Give the extent of all uninfected red blood cells.
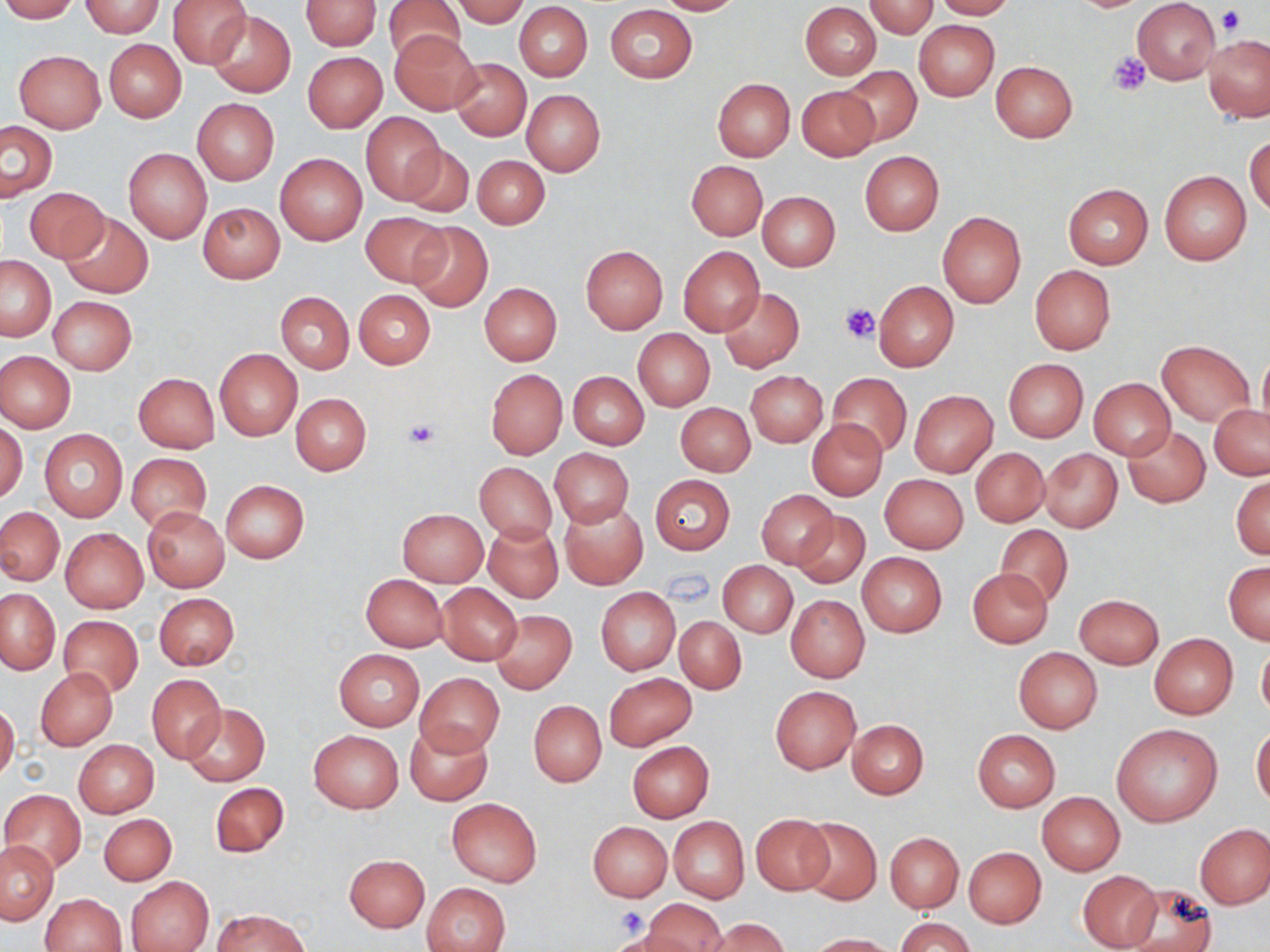
Approximate bounding boxes as [x1, y1, x2, y2] in pixels.
Uninfected red blood cells: [0, 0, 79, 22], [168, 0, 253, 69], [385, 0, 465, 66], [453, 0, 529, 26], [654, 0, 742, 15], [932, 0, 1016, 19], [1133, 0, 1221, 85], [82, 1, 164, 37], [300, 1, 381, 50], [864, 1, 936, 38], [514, 3, 592, 81], [800, 3, 882, 80], [605, 4, 698, 83], [206, 9, 296, 99], [914, 19, 999, 101], [390, 32, 481, 114], [1203, 34, 1270, 122], [104, 39, 186, 121], [14, 50, 106, 133], [303, 52, 387, 132], [450, 58, 531, 140], [990, 60, 1078, 141], [838, 65, 921, 146], [712, 77, 795, 161], [796, 85, 879, 161], [522, 89, 605, 175], [192, 99, 279, 184], [361, 114, 447, 204], [1, 122, 57, 201], [1246, 133, 1270, 217], [400, 144, 474, 218], [124, 148, 212, 243], [860, 151, 944, 235], [276, 152, 367, 245], [473, 155, 549, 229], [687, 161, 767, 240], [1160, 171, 1251, 265], [1063, 184, 1153, 268], [25, 188, 108, 262], [758, 191, 840, 270], [198, 201, 285, 284], [937, 210, 1027, 308], [359, 211, 450, 289], [61, 212, 152, 297], [406, 221, 493, 311], [581, 245, 668, 333], [678, 246, 764, 335], [0, 255, 55, 341], [1029, 264, 1116, 355], [873, 281, 959, 371], [479, 282, 562, 365], [721, 288, 804, 373], [353, 289, 436, 368], [277, 292, 353, 373], [49, 297, 136, 375], [632, 329, 714, 411], [1157, 342, 1253, 425], [214, 349, 302, 440], [1258, 349, 1270, 437], [0, 350, 75, 433], [1004, 360, 1088, 442], [486, 369, 567, 458], [745, 371, 828, 447], [568, 372, 649, 449], [134, 373, 219, 451], [828, 373, 911, 456], [1088, 378, 1175, 458], [909, 391, 997, 476], [290, 392, 371, 475], [676, 402, 755, 476], [1209, 404, 1269, 478], [808, 419, 887, 500], [1, 422, 27, 504], [1124, 425, 1212, 508], [40, 429, 127, 521], [971, 447, 1050, 527], [550, 448, 634, 528], [1039, 449, 1122, 533], [126, 453, 212, 532], [474, 462, 556, 543], [879, 473, 968, 554], [1231, 474, 1269, 559], [651, 475, 736, 554], [221, 480, 310, 563], [757, 489, 839, 570], [558, 501, 647, 590], [1, 507, 65, 585], [142, 507, 229, 592], [397, 508, 488, 587], [793, 511, 869, 590], [483, 521, 563, 603], [994, 524, 1075, 608], [60, 528, 148, 612], [857, 552, 946, 637], [1223, 561, 1270, 643], [719, 562, 797, 635], [968, 567, 1054, 647], [361, 574, 447, 651], [437, 583, 522, 665], [595, 587, 681, 675], [0, 589, 60, 673], [154, 593, 238, 670], [786, 594, 869, 683], [1074, 594, 1163, 669], [491, 610, 577, 694], [57, 615, 143, 697], [674, 617, 746, 694], [1149, 633, 1238, 719], [1257, 641, 1270, 724], [1013, 647, 1102, 733], [333, 649, 424, 730], [36, 668, 118, 749], [416, 672, 504, 756], [147, 673, 226, 763], [605, 673, 697, 751], [770, 686, 861, 773], [529, 701, 606, 787], [0, 702, 20, 783], [183, 703, 269, 786], [846, 719, 928, 799], [405, 722, 490, 804], [1111, 723, 1223, 826], [1251, 726, 1270, 810], [308, 729, 403, 812], [973, 729, 1061, 812], [74, 740, 158, 817], [627, 741, 714, 822], [210, 782, 288, 857], [2, 789, 86, 874], [1038, 792, 1125, 875], [448, 797, 541, 886], [99, 813, 176, 885], [750, 814, 835, 897], [795, 815, 883, 905], [668, 817, 749, 902], [588, 822, 672, 901], [1195, 823, 1270, 908], [885, 831, 963, 913], [883, 840, 1044, 919], [0, 841, 58, 924], [965, 847, 1046, 927], [344, 853, 429, 932], [1078, 870, 1163, 949], [348, 871, 510, 943], [126, 877, 214, 952], [420, 882, 510, 952], [1119, 882, 1216, 952], [42, 893, 127, 952], [645, 898, 726, 951], [213, 909, 308, 952], [897, 917, 974, 952], [710, 918, 789, 952], [808, 933, 895, 951].

Platelet locations: [1218, 6, 1247, 35], [1108, 52, 1152, 94], [839, 302, 880, 343], [405, 417, 441, 448], [614, 906, 647, 939]. Slide-level diagnosis: no evidence of blood parasites. Thin blood smear. May-Grünwald-Giemsa stain. Optical microscopy. Image is 1270×952 pixels. Captured at 1000x magnification. One field of a larger specimen.